Give the extent of all Plasmodium parasites.
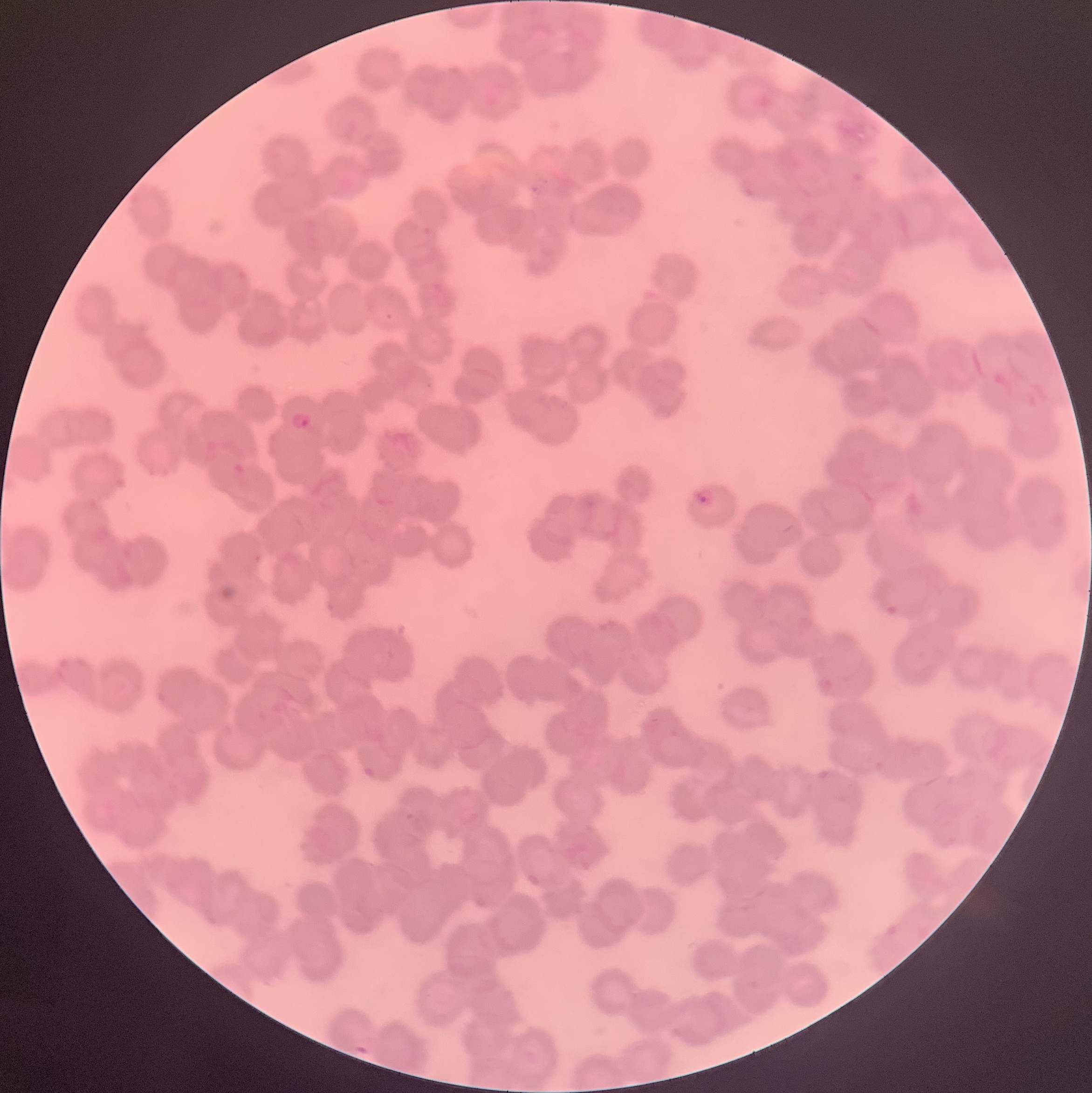

Approximate bounding boxes as (x1, y1, x2, y2) in pixels.
Plasmodium parasites: (288, 410, 313, 431), (692, 487, 716, 509).

Thin blood film. Light microscopy. Image is 1092×1093 pixels. The red blood cells show rouleaux formation.